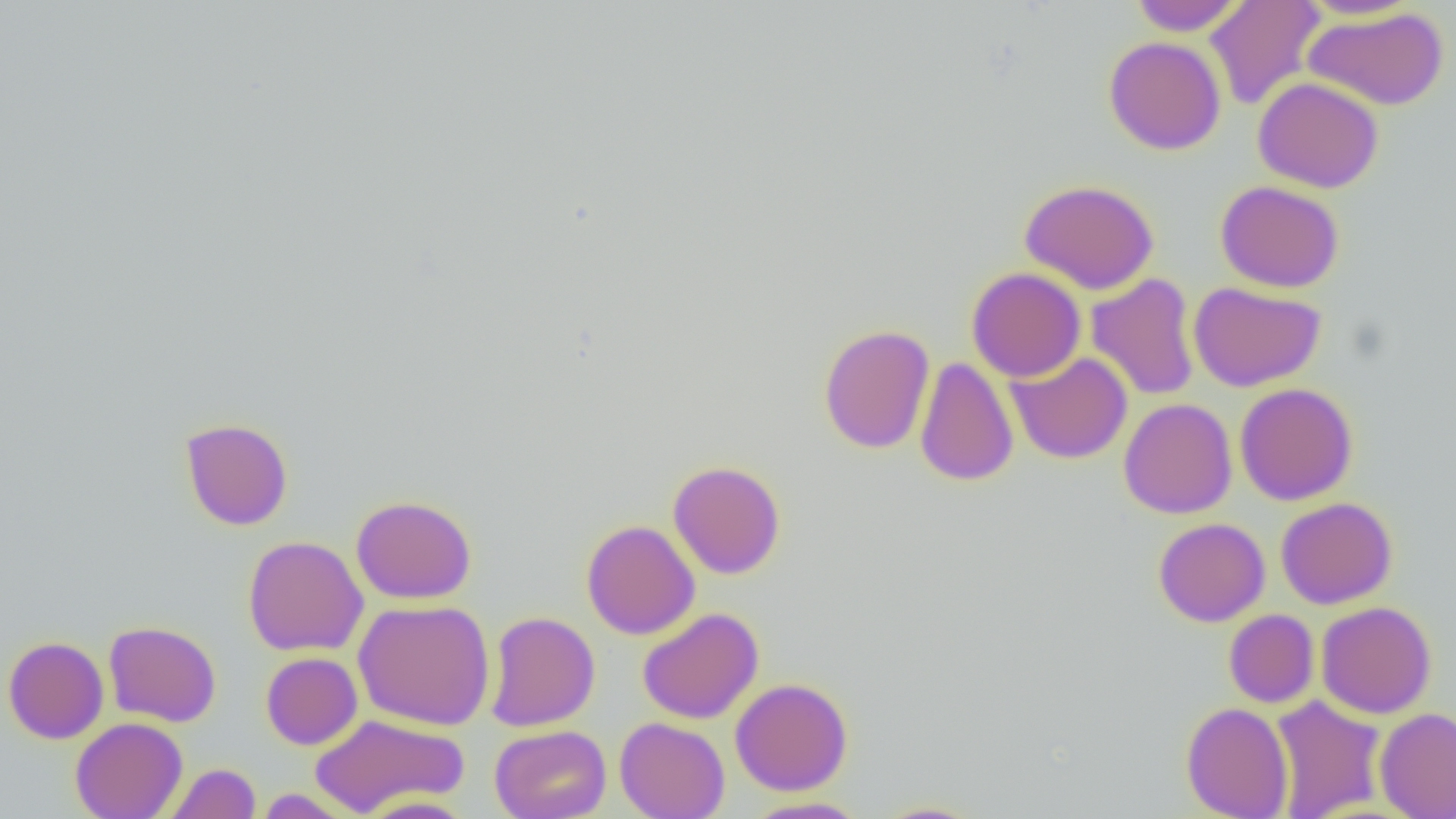
slide-level diagnosis = no evidence of blood parasites
preparation = thin blood film
field of view = single
image size = 1456×819 pixels
magnification = 1000x
modality = light microscopy
uninfected red blood cell locations = approximate bounding boxes as [x1, y1, x2, y2] in pixels: [1130, 0, 1244, 36], [1205, 0, 1326, 111], [1296, 0, 1422, 20], [1304, 7, 1449, 111], [1103, 36, 1227, 155], [1253, 76, 1384, 193], [1020, 179, 1159, 295], [1215, 180, 1345, 293], [966, 267, 1086, 382], [1086, 273, 1201, 402], [1188, 281, 1327, 392], [818, 323, 935, 454], [1006, 352, 1132, 464], [915, 356, 1019, 487], [1234, 383, 1358, 505], [1119, 398, 1238, 519], [180, 417, 293, 531], [668, 460, 786, 579], [351, 495, 477, 604], [1275, 497, 1397, 609], [1153, 518, 1270, 627], [580, 519, 700, 640], [242, 535, 369, 656], [353, 599, 495, 730], [1316, 601, 1437, 719], [637, 607, 763, 724], [1223, 609, 1319, 708], [484, 611, 599, 731], [103, 620, 222, 727], [2, 636, 109, 744], [260, 652, 362, 749], [730, 678, 853, 795], [1270, 695, 1387, 819], [1180, 702, 1293, 819], [1374, 707, 1456, 819], [309, 713, 469, 817], [615, 716, 730, 819], [70, 717, 188, 819], [489, 724, 611, 819], [164, 763, 260, 819], [254, 789, 357, 818], [359, 795, 476, 819], [742, 796, 870, 819], [871, 800, 987, 818]